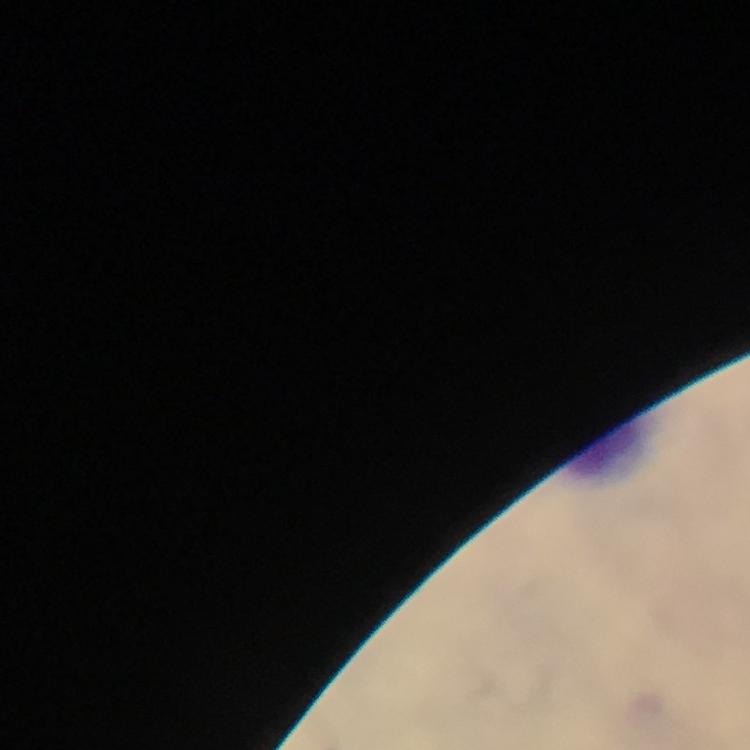
Approximate centers as {x, y} in pixels.
Summary:
  - Leukocyte locations: {610, 452}
  - Image size: 750×750 pixels
  - Stain: Giemsa
  - Plasmodium parasites: none seen
  - Magnification: 100x
  - Immersion oil: applied
  - Cropped from: a single field of view
  - Capture: smartphone mounted on the microscope
  - Context: from a malaria diagnostic workup
  - Preparation: thick blood film